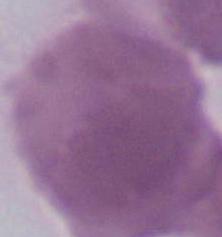 1000x magnification. A red blood cell is seen. Photomicrograph.